Outline each Plasmodium falciparum-infected red blood cell.
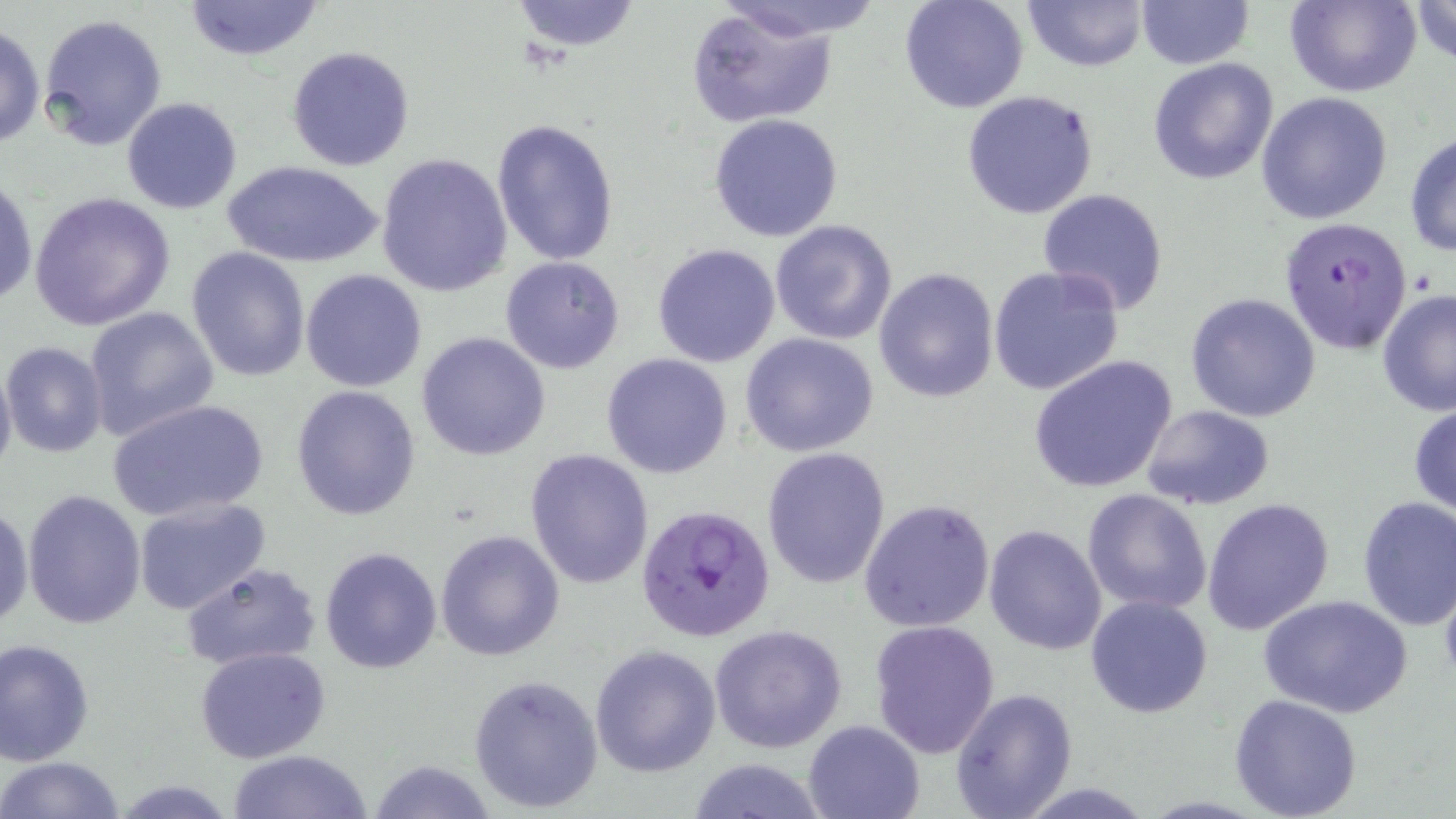
Approximate bounding boxes as [x1, y1, x2, y2] in pixels.
Plasmodium falciparum-infected red blood cells: [1278, 214, 1414, 356], [636, 503, 774, 642].

Summary:
  - Uninfected red blood cell locations: [181, 0, 327, 61], [508, 0, 643, 53], [710, 0, 885, 43], [899, 0, 1030, 114], [1021, 0, 1148, 73], [1284, 0, 1421, 97], [1408, 0, 1456, 65], [1135, 1, 1255, 71], [685, 7, 842, 128], [38, 13, 169, 152], [1, 23, 46, 150], [286, 44, 416, 172], [1146, 57, 1279, 185], [960, 89, 1100, 220], [1255, 91, 1393, 224], [119, 96, 244, 215], [708, 114, 845, 242], [491, 119, 621, 265], [1405, 131, 1456, 259], [375, 152, 515, 296], [228, 161, 380, 268], [0, 172, 38, 311], [1037, 187, 1169, 314], [27, 190, 177, 332], [769, 219, 898, 346], [651, 242, 781, 368], [187, 247, 311, 381], [501, 256, 625, 374], [988, 265, 1127, 397], [873, 266, 1000, 403], [300, 268, 428, 393], [1377, 288, 1456, 416], [1185, 292, 1321, 422], [82, 306, 219, 442], [416, 332, 551, 461], [740, 333, 881, 459], [2, 342, 108, 457], [600, 352, 734, 479], [1028, 355, 1178, 494], [0, 356, 17, 488], [289, 386, 421, 520], [106, 398, 270, 523], [1409, 400, 1456, 521], [1141, 405, 1276, 511], [761, 447, 892, 589], [524, 448, 655, 589], [1081, 488, 1212, 615], [22, 490, 148, 631], [131, 494, 272, 615], [1356, 496, 1456, 630], [858, 498, 996, 634], [1201, 498, 1335, 634], [0, 502, 32, 634], [984, 524, 1108, 655], [434, 529, 566, 663], [319, 546, 443, 674], [180, 561, 322, 671], [1086, 593, 1215, 718], [1259, 596, 1411, 718], [869, 619, 1000, 758], [709, 624, 846, 754], [1, 637, 96, 764], [590, 643, 721, 777], [194, 647, 333, 764], [467, 673, 602, 813], [949, 686, 1077, 819], [1229, 694, 1363, 819], [802, 719, 926, 818], [225, 750, 374, 819], [0, 755, 127, 818], [681, 757, 834, 818], [366, 759, 500, 818], [113, 779, 237, 817]
  - Slide-level diagnosis: Plasmodium falciparum
  - Stain: May-Grünwald-Giemsa
  - Field of view: single
  - Modality: optical microscopy
  - Preparation: thin blood smear
  - Magnification: 1000x
  - Image size: 1456×819 pixels